Name the blood parasite species.
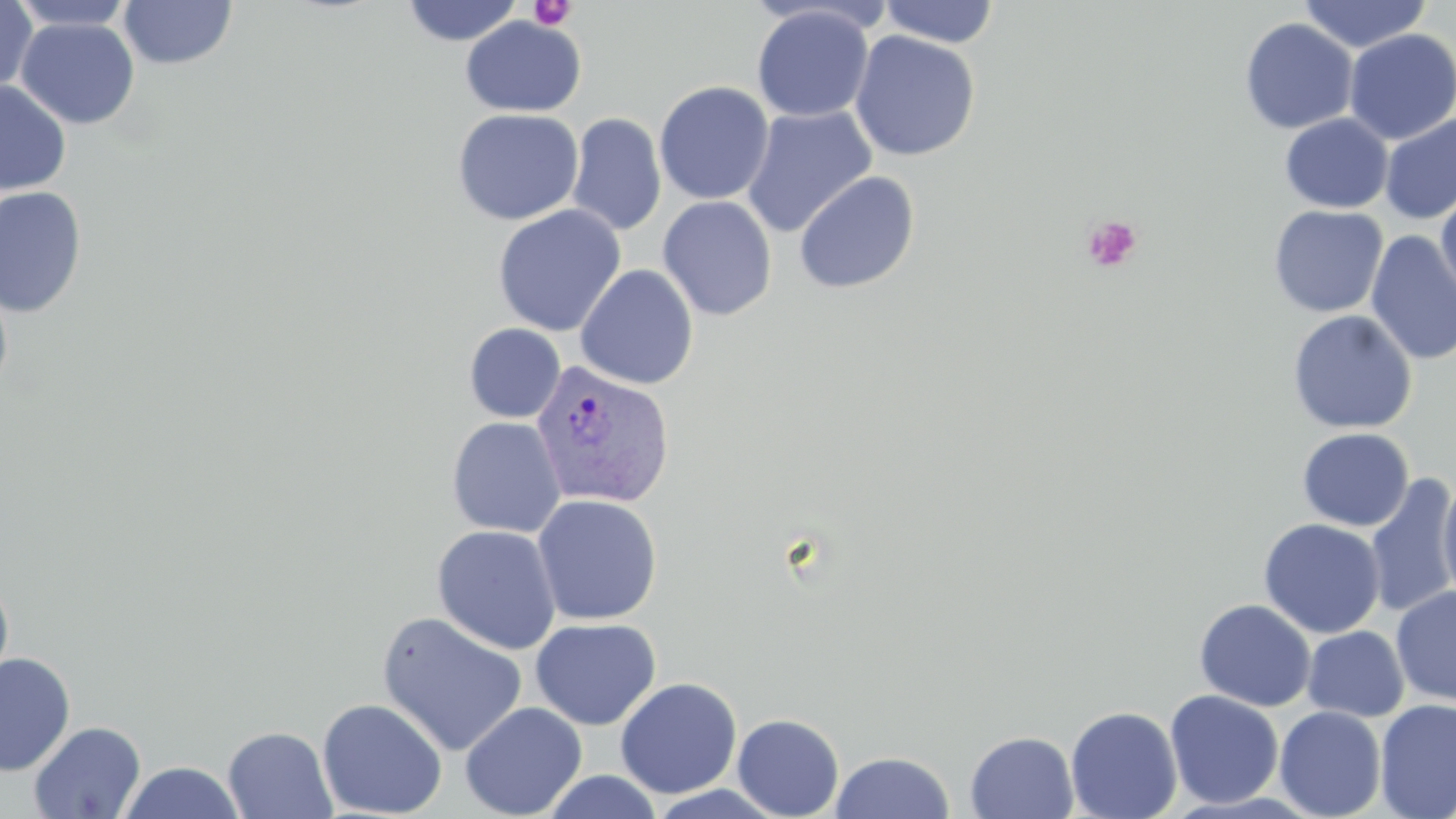
Plasmodium vivax.

Approximate bounding boxes as [x1, y1, x2, y2] in pixels. Uninfected red blood cell locations: [8, 0, 137, 31], [118, 0, 237, 70], [1298, 0, 1431, 54], [0, 1, 37, 95], [400, 1, 524, 46], [877, 1, 1001, 48], [752, 5, 874, 122], [460, 16, 587, 117], [14, 18, 141, 131], [1239, 18, 1358, 135], [1343, 29, 1456, 144], [849, 31, 981, 162], [0, 80, 71, 195], [654, 81, 775, 205], [742, 106, 877, 238], [452, 108, 584, 226], [566, 113, 667, 237], [1279, 113, 1393, 213], [1380, 113, 1456, 224], [793, 171, 920, 294], [0, 185, 87, 319], [1436, 186, 1456, 307], [657, 195, 777, 321], [492, 205, 627, 336], [1268, 205, 1388, 318], [1365, 230, 1456, 365], [575, 264, 699, 390], [0, 276, 14, 400], [1287, 310, 1417, 434], [464, 323, 566, 423], [446, 416, 566, 537], [1296, 427, 1414, 531], [1437, 471, 1456, 611], [1364, 473, 1456, 619], [532, 494, 663, 625], [1258, 518, 1386, 639], [431, 524, 562, 655], [0, 571, 14, 695], [1391, 586, 1456, 706], [1194, 598, 1316, 712], [376, 610, 529, 756], [530, 617, 662, 731], [1302, 626, 1409, 722], [0, 652, 75, 776], [615, 677, 742, 799], [1165, 690, 1284, 809], [317, 697, 448, 818], [1375, 699, 1456, 819], [459, 701, 588, 819], [1065, 705, 1183, 818], [1274, 706, 1387, 819], [732, 713, 844, 818], [28, 720, 146, 818], [223, 726, 337, 818], [965, 731, 1079, 818], [830, 750, 955, 818], [116, 761, 248, 819], [541, 770, 665, 818], [645, 785, 787, 818]. Platelet locations: [528, 0, 577, 31], [1082, 215, 1143, 272]. Plasmodium vivax-infected red blood cell locations: [530, 359, 675, 510]. 1000x magnification. Light microscopy. Single field of view. Image is 1456×819 pixels. May-Grünwald-Giemsa stain. Thin blood smear.